State the blood parasite species.
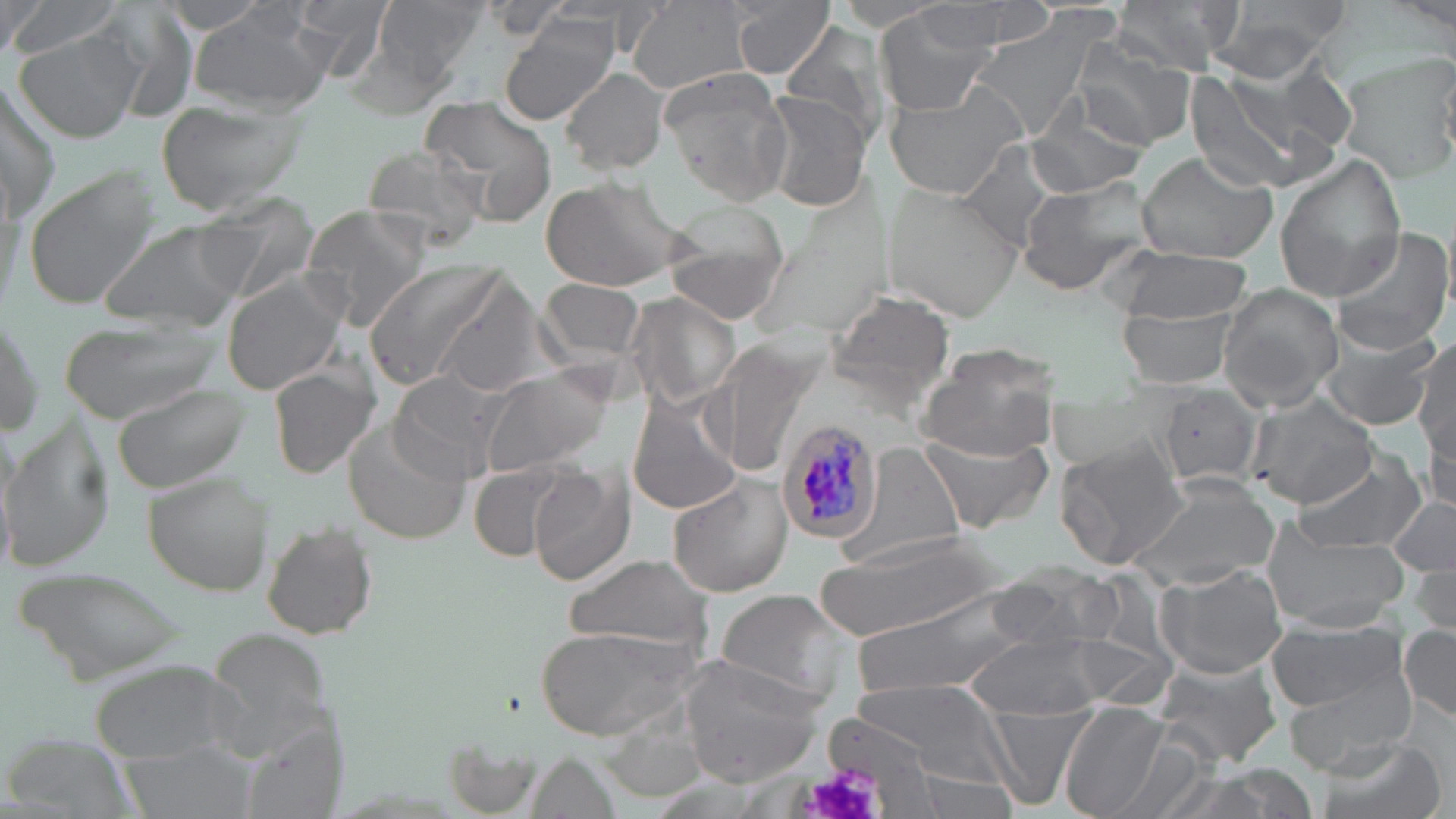

Plasmodium malariae.

field_of_view: single
magnification: 1000x
image_size: 1456×819 pixels
modality: optical microscopy
preparation: thin blood film
plasmodium_malariae_infected_red_blood_cell_locations: 'approximate bounding boxes as [x1, y1, x2, y2] in pixels: [776, 417, 884, 545]'
uninfected_red_blood_cell_locations: 'approximate bounding boxes as [x1, y1, x2, y2] in pixels: [163, 0, 275, 34], [293, 0, 397, 76], [377, 0, 486, 83], [726, 0, 835, 79], [900, 0, 1057, 59], [7, 1, 121, 59], [483, 1, 571, 40], [626, 1, 755, 93], [1111, 1, 1236, 79], [0, 2, 45, 54], [1209, 2, 1351, 80], [873, 5, 998, 116], [962, 8, 1120, 148], [191, 9, 333, 111], [498, 15, 620, 125], [781, 21, 891, 145], [13, 31, 144, 144], [1076, 33, 1198, 151], [1335, 51, 1456, 186], [1251, 60, 1358, 159], [560, 65, 671, 174], [1183, 66, 1320, 197], [661, 68, 793, 205], [0, 78, 62, 220], [882, 80, 1029, 202], [761, 90, 875, 214], [1026, 93, 1150, 199], [420, 94, 557, 222], [154, 99, 304, 218], [952, 139, 1074, 255], [360, 142, 490, 254], [1139, 151, 1279, 266], [1274, 154, 1408, 302], [20, 165, 163, 311], [1015, 173, 1157, 297], [539, 176, 686, 293], [886, 181, 1027, 321], [196, 193, 321, 300], [661, 198, 791, 326], [300, 204, 430, 331], [102, 219, 244, 332], [1328, 226, 1455, 358], [1112, 246, 1252, 325], [360, 258, 509, 393], [222, 272, 348, 393], [434, 277, 552, 400], [540, 277, 648, 367], [1217, 284, 1343, 412], [823, 290, 956, 406], [627, 292, 739, 411], [1121, 304, 1237, 387], [0, 308, 46, 438], [55, 314, 221, 424], [1315, 332, 1443, 432], [702, 334, 822, 479], [921, 339, 1063, 460], [1412, 339, 1455, 454], [268, 362, 380, 479], [477, 363, 617, 480], [389, 370, 510, 483], [111, 378, 250, 493], [1156, 384, 1264, 493], [628, 393, 740, 516], [1245, 394, 1379, 509], [1423, 407, 1455, 515], [3, 415, 116, 570], [344, 416, 474, 545], [921, 432, 1056, 536], [1054, 439, 1190, 570], [839, 441, 972, 568], [1295, 446, 1425, 554], [468, 459, 575, 559], [529, 466, 635, 584], [143, 469, 272, 596], [668, 473, 794, 598], [1122, 477, 1280, 591], [1388, 496, 1455, 582], [261, 516, 379, 641], [1264, 527, 1406, 632], [817, 532, 1004, 647], [564, 552, 713, 652], [10, 562, 193, 684], [1154, 562, 1288, 680], [987, 565, 1126, 649], [1411, 566, 1452, 638], [716, 587, 854, 705], [844, 593, 1027, 700], [1267, 619, 1413, 727], [1400, 624, 1456, 722], [534, 625, 700, 741], [206, 626, 336, 753], [966, 631, 1116, 721], [1062, 632, 1178, 710], [680, 657, 832, 787], [1151, 657, 1280, 768], [1275, 658, 1421, 774], [88, 659, 246, 764], [849, 680, 1016, 782], [1059, 701, 1176, 819], [982, 702, 1093, 810], [247, 725, 342, 819], [1109, 734, 1214, 819], [1310, 734, 1448, 819], [126, 745, 255, 819]'
stain: May-Grünwald-Giemsa